Report the malaria status of this cell.
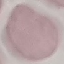

It is uninfected.

Automatically extracted cell patch, resized to 64 × 64 pixels. Thin blood film. Giemsa-stained preparation. Acquired by smartphone through the microscope eyepiece.